Mark where white blood cells are.
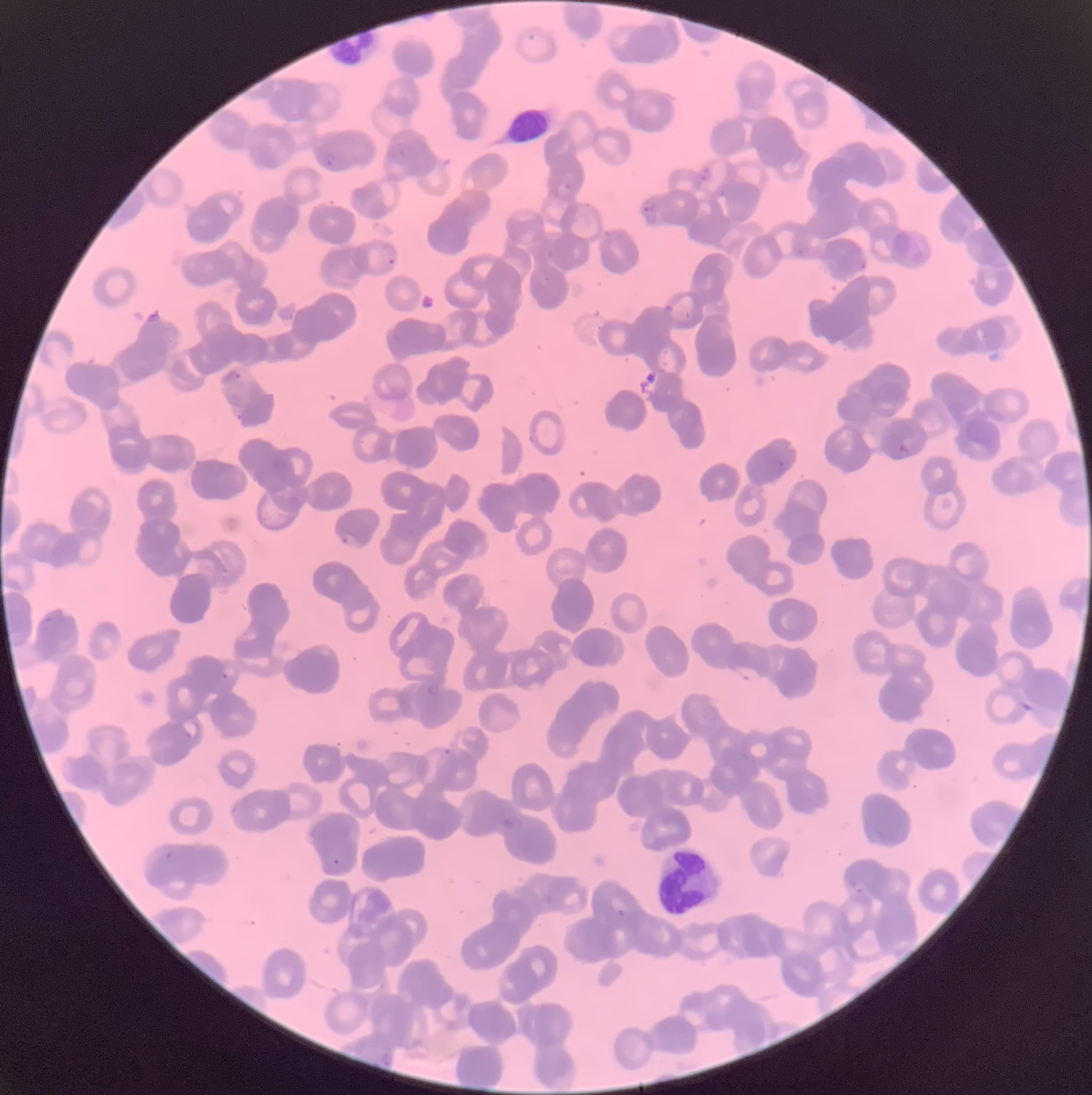
Approximate bounding boxes as named x1/y1/x2/y2 corners in pixels.
White blood cells: (x1=327, y1=31, x2=386, y2=68), (x1=505, y1=108, x2=552, y2=141), (x1=658, y1=849, x2=725, y2=914).

Plasmodium parasites too small for a box (approximate object centers, named x/y in pixels) = (x=550, y=254), (x=864, y=265), (x=547, y=279), (x=781, y=463), (x=48, y=619), (x=225, y=676), (x=860, y=891)
Plasmodium parasite locations = (x1=324, y1=153, x2=337, y2=167), (x1=558, y1=183, x2=573, y2=196), (x1=640, y1=202, x2=657, y2=213), (x1=381, y1=246, x2=398, y2=265), (x1=796, y1=250, x2=804, y2=255), (x1=224, y1=371, x2=242, y2=382), (x1=236, y1=414, x2=244, y2=421), (x1=898, y1=443, x2=910, y2=453), (x1=341, y1=532, x2=361, y2=547), (x1=732, y1=665, x2=762, y2=682), (x1=428, y1=684, x2=441, y2=696), (x1=178, y1=717, x2=202, y2=742), (x1=443, y1=748, x2=453, y2=756), (x1=503, y1=818, x2=516, y2=831), (x1=166, y1=850, x2=174, y2=859), (x1=332, y1=859, x2=342, y2=866), (x1=617, y1=909, x2=626, y2=917)
preparation = thin blood film
image size = 1092×1095 pixels
red blood cell morphology = rouleaux formation
modality = optical microscopy